Report the malaria status of this cell.
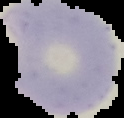
Parasitized.

image_type: cell region segmented out of the field of view; surrounding area masked to black
preparation: thin blood smear
image_size: 124×118 pixels